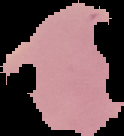
Summary:
  - Image size: 124×136 pixels
  - Result: Plasmodium parasites identified
  - Preparation: thin blood smear
  - Image type: segmented cell region with the area outside set to black